Classify this cell by malaria status.
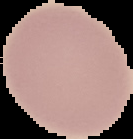

Uninfected.

image size = 133×139 pixels
image type = cell region segmented out of the field of view; surrounding area masked to black
preparation = thin blood film